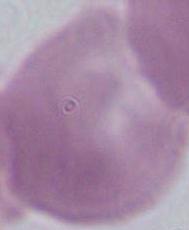
An erythrocyte is seen. Captured at 1000x magnification. Micrograph.